Report the malaria status of this cell.
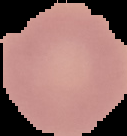

It is uninfected.

Summary:
  - Preparation: thin blood film
  - Image type: cell region segmented out of the field of view; surrounding area masked to black
  - Image size: 127×136 pixels